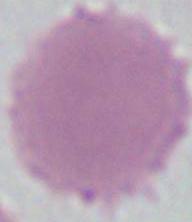
Summary:
  - Identification: erythrocyte
  - Modality: micrograph
  - Magnification: 1000x